Outline each uninfected red blood cell.
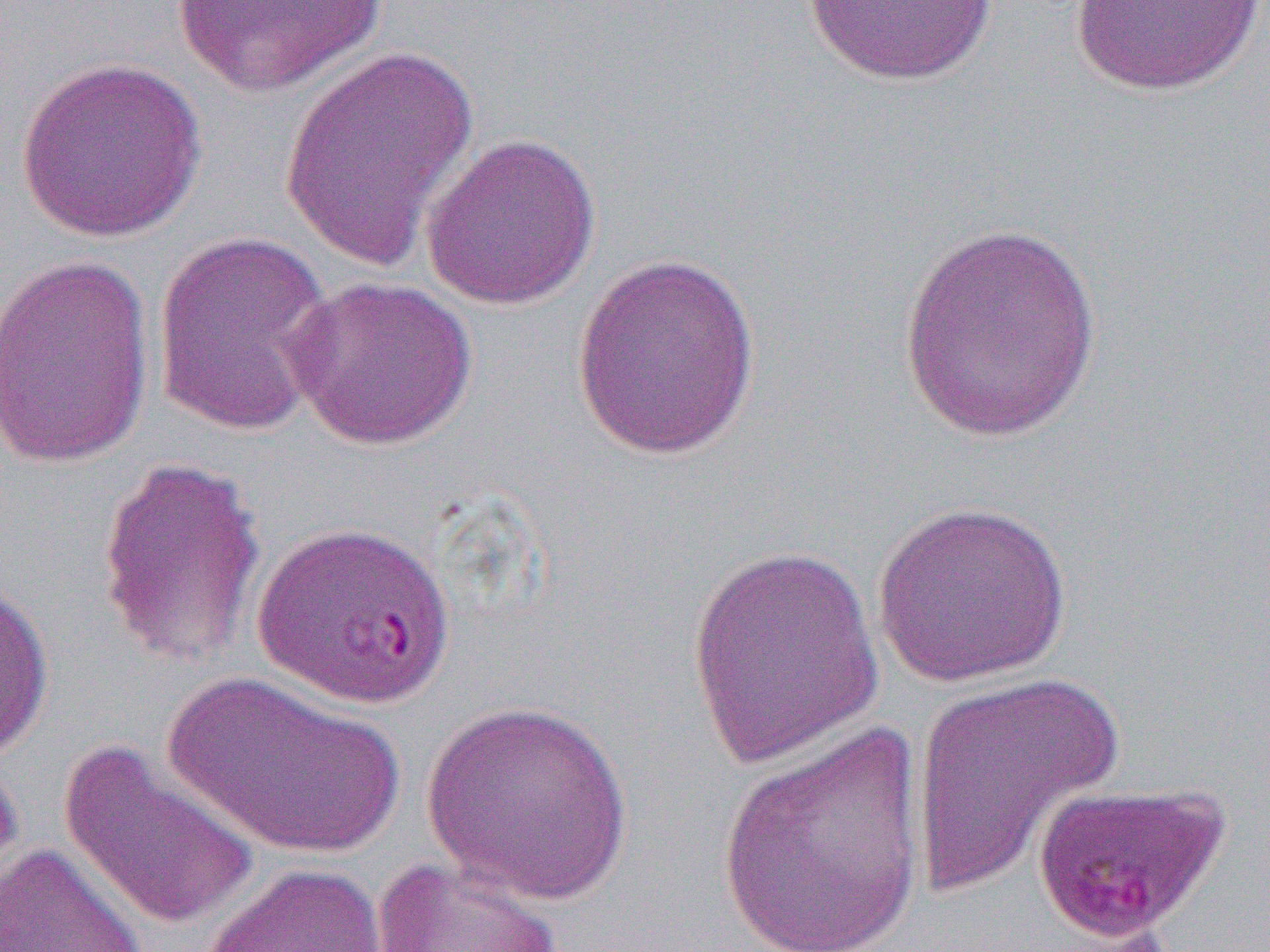

Approximate bounding boxes as (x1, y1, x2, y2) in pixels.
Uninfected red blood cells (subset): (164, 0, 396, 99), (802, 0, 998, 86), (1069, 1, 1265, 96), (278, 47, 478, 273), (14, 57, 207, 242), (420, 133, 601, 310), (897, 218, 1102, 444), (151, 230, 339, 437), (569, 252, 763, 462), (1, 253, 155, 471), (284, 276, 479, 451), (96, 453, 267, 668), (871, 500, 1073, 687), (683, 544, 887, 766), (0, 573, 54, 762), (162, 671, 407, 860), (908, 671, 1126, 899), (419, 700, 636, 905), (718, 723, 926, 952), (58, 739, 260, 932), (0, 756, 26, 916), (0, 842, 148, 952), (370, 855, 566, 952), (201, 862, 389, 952).

Summary:
  - Slide-level diagnosis: Plasmodium falciparum
  - Modality: light microscopy
  - Magnification: 1000x
  - Field of view: single
  - Image size: 1270×952 pixels
  - Preparation: thin blood smear